Locate every leukocyte (white blood cell).
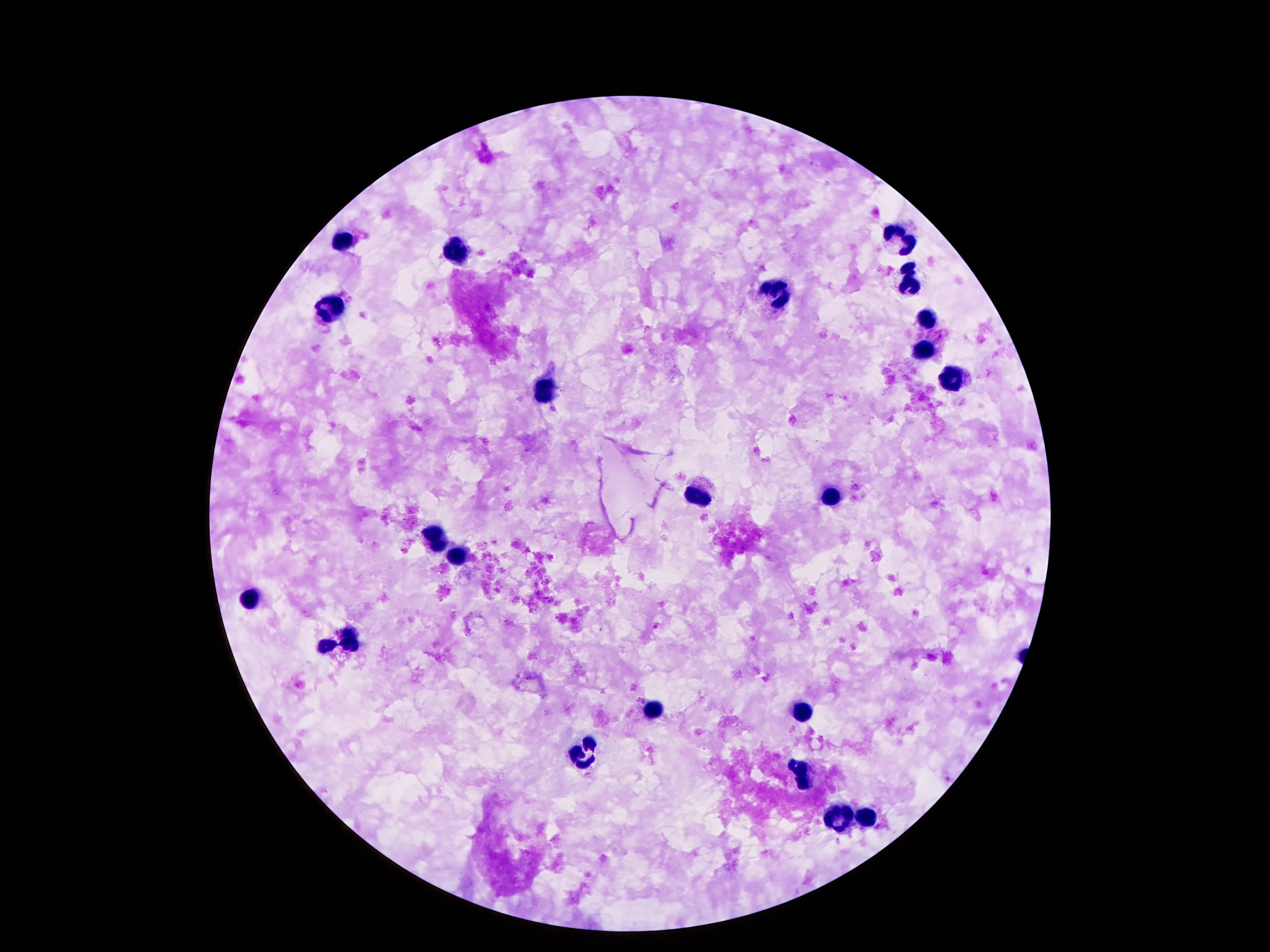
Approximate centers as [x, y] in pixels.
Leukocytes: [343, 238], [905, 241], [457, 251], [912, 281], [778, 294], [332, 305], [927, 316], [924, 354], [957, 381], [545, 389], [698, 495], [832, 500], [435, 544], [459, 557], [250, 600], [351, 639], [328, 647], [653, 708], [802, 711], [582, 753], [802, 773], [868, 816], [834, 818].

capture = smartphone camera through the microscope eyepiece
preparation = thick blood smear
image size = 1270×952 pixels
patient malaria status = negative
stain = Giemsa
magnification = 100x
field of view = single